Identify the parasite.
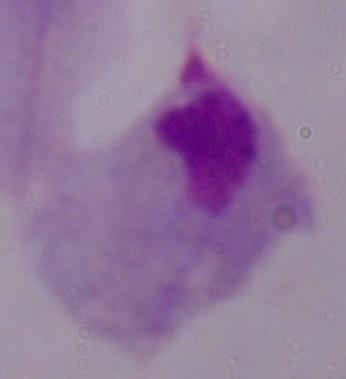

This is a trichomonad.

1000x magnification. Micrograph.